Classify this cell by malaria status.
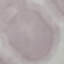

Uninfected.

{
  "capture": "smartphone camera at the microscope eyepiece",
  "image_type": "automatically extracted cell patch, resized to 64 × 64 pixels",
  "stain": "Giemsa",
  "preparation": "thin blood film"
}